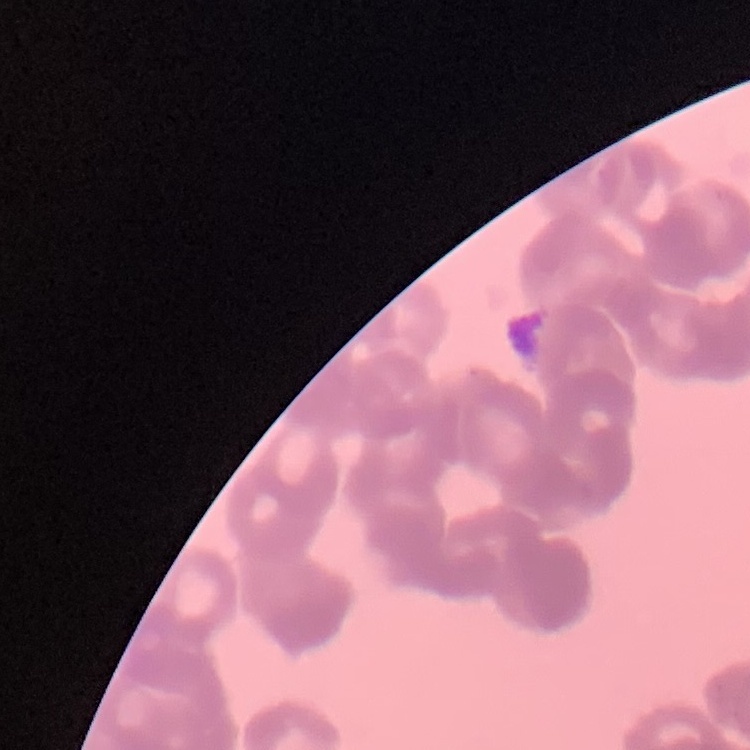
{
  "erythrocyte_morphology": "rouleaux formation",
  "preparation": "thin blood film",
  "stain": "Field's or Giemsa",
  "image_type": "one tile cut from a larger photomicrograph"
}